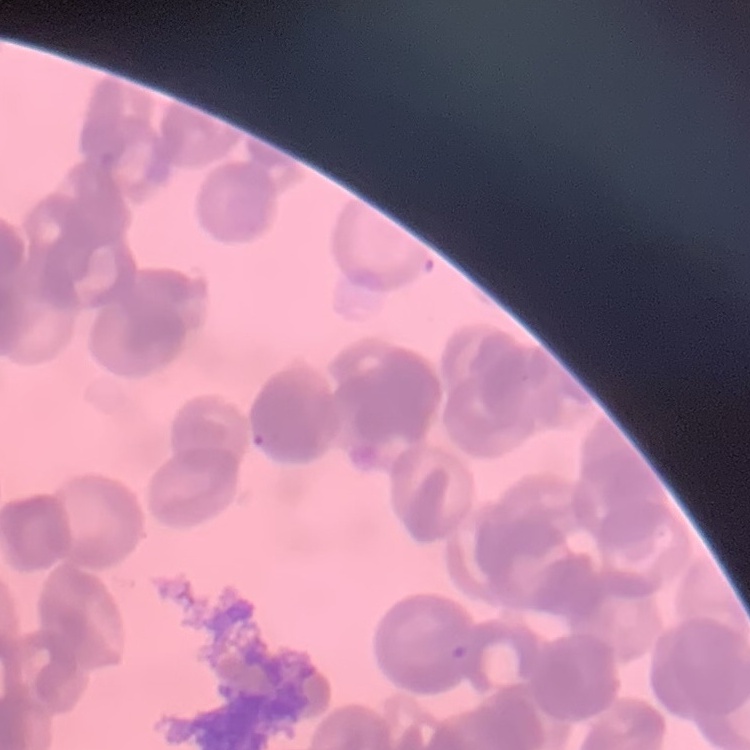
red_blood_cell_morphology: rouleaux formation
stain: Field's or Giemsa
preparation: thin blood smear
image_type: square crop of a larger photomicrograph